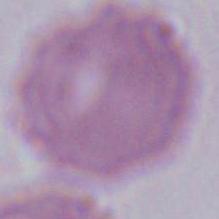

Summary:
  - Modality: photomicrograph
  - Magnification: 1000x
  - Identification: erythrocyte